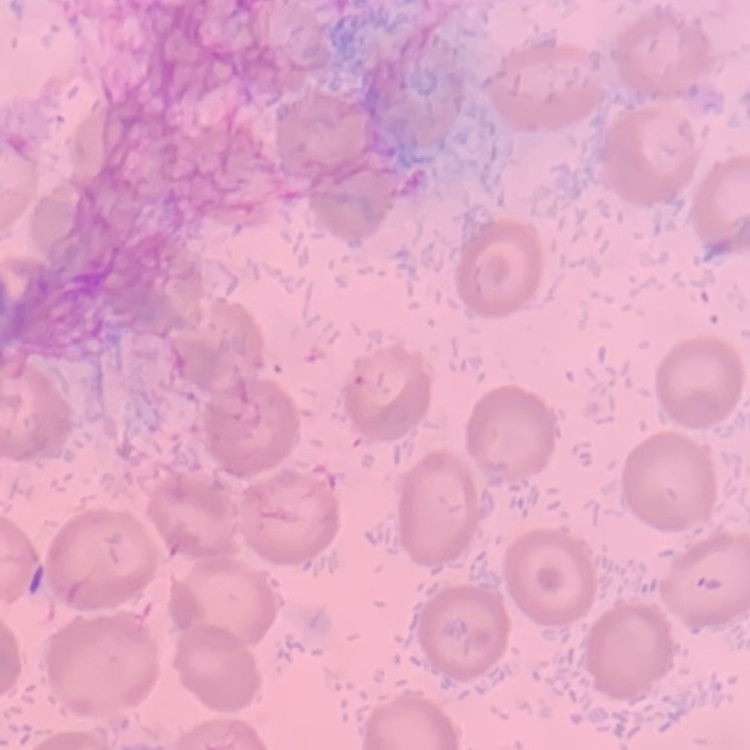

erythrocyte morphology = no rouleaux formation
preparation = thin blood smear
image type = square crop of a larger photomicrograph
stain = Field's or Giemsa